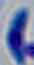
modality: micrograph
magnification: 1000x
identification: Toxoplasma gondii